Report the malaria status of this cell.
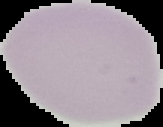
It is uninfected.

Summary:
  - Image size: 163×127 pixels
  - Preparation: thin blood film
  - Image type: segmented cell region on a black background